State which parasite is depicted.
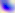

Toxoplasma gondii.

magnification = 400x
modality = micrograph